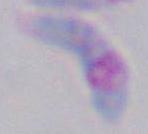
Summary:
  - Magnification: 1000x
  - Identification: Toxoplasma gondii
  - Modality: photomicrograph